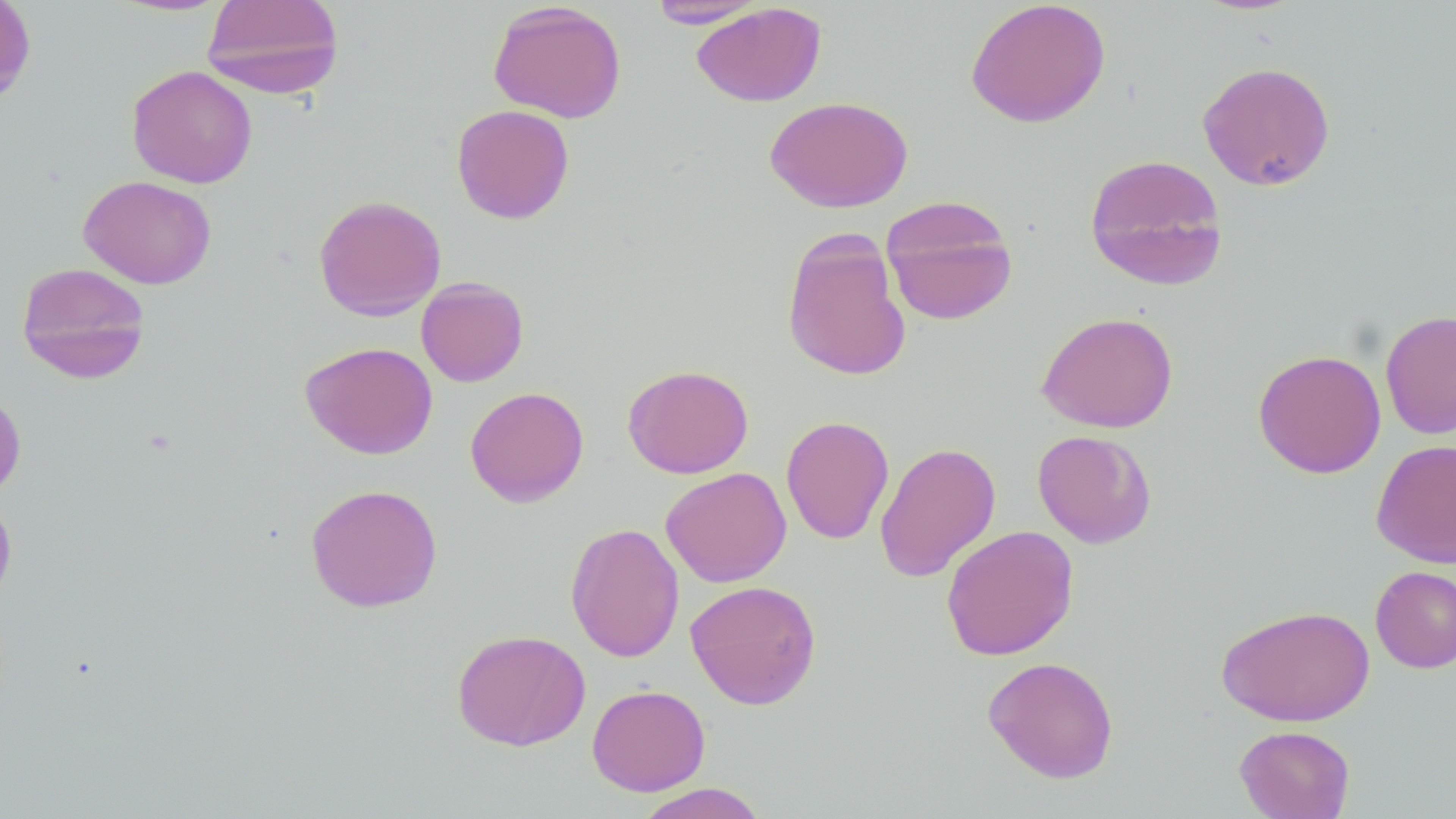
slide-level diagnosis = negative for blood parasites
modality = light microscopy
field of view = single
image size = 1456×819 pixels
preparation = thin blood film
stain = May-Grünwald-Giemsa
magnification = 1000x
uninfected red blood cell locations = approximate bounding boxes as named x1/y1/x2/y2 corners in pixels: (x1=0, y1=0, x2=36, y2=106), (x1=201, y1=0, x2=345, y2=99), (x1=965, y1=0, x2=1111, y2=128), (x1=647, y1=1, x2=767, y2=28), (x1=488, y1=2, x2=627, y2=123), (x1=691, y1=2, x2=827, y2=107), (x1=1197, y1=60, x2=1336, y2=191), (x1=126, y1=65, x2=258, y2=188), (x1=765, y1=96, x2=912, y2=212), (x1=451, y1=104, x2=575, y2=224), (x1=1084, y1=152, x2=1229, y2=291), (x1=78, y1=175, x2=216, y2=289), (x1=313, y1=194, x2=447, y2=321), (x1=881, y1=195, x2=1018, y2=326), (x1=781, y1=228, x2=911, y2=382), (x1=16, y1=261, x2=151, y2=384), (x1=415, y1=276, x2=529, y2=387), (x1=1380, y1=309, x2=1456, y2=440), (x1=1036, y1=311, x2=1178, y2=433), (x1=299, y1=341, x2=438, y2=460), (x1=1253, y1=349, x2=1386, y2=479), (x1=622, y1=364, x2=754, y2=478), (x1=465, y1=386, x2=589, y2=507), (x1=0, y1=389, x2=27, y2=502), (x1=780, y1=415, x2=894, y2=545), (x1=1032, y1=429, x2=1157, y2=549), (x1=1371, y1=439, x2=1456, y2=568), (x1=874, y1=441, x2=1001, y2=582), (x1=660, y1=467, x2=792, y2=588), (x1=305, y1=482, x2=443, y2=612), (x1=0, y1=496, x2=17, y2=608), (x1=565, y1=522, x2=685, y2=663), (x1=940, y1=524, x2=1079, y2=661), (x1=1370, y1=565, x2=1456, y2=673), (x1=685, y1=579, x2=822, y2=710), (x1=1216, y1=604, x2=1375, y2=727), (x1=451, y1=628, x2=591, y2=752), (x1=982, y1=656, x2=1120, y2=783), (x1=587, y1=684, x2=711, y2=796), (x1=1234, y1=724, x2=1355, y2=819), (x1=633, y1=783, x2=768, y2=819)